Classify this cell by malaria status.
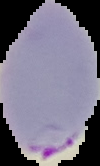

Parasitized.

From a thin blood smear. Cell region segmented out of the field of view; the surrounding area is masked to black. Image is 100×166 pixels.